Point out each Plasmodium parasite.
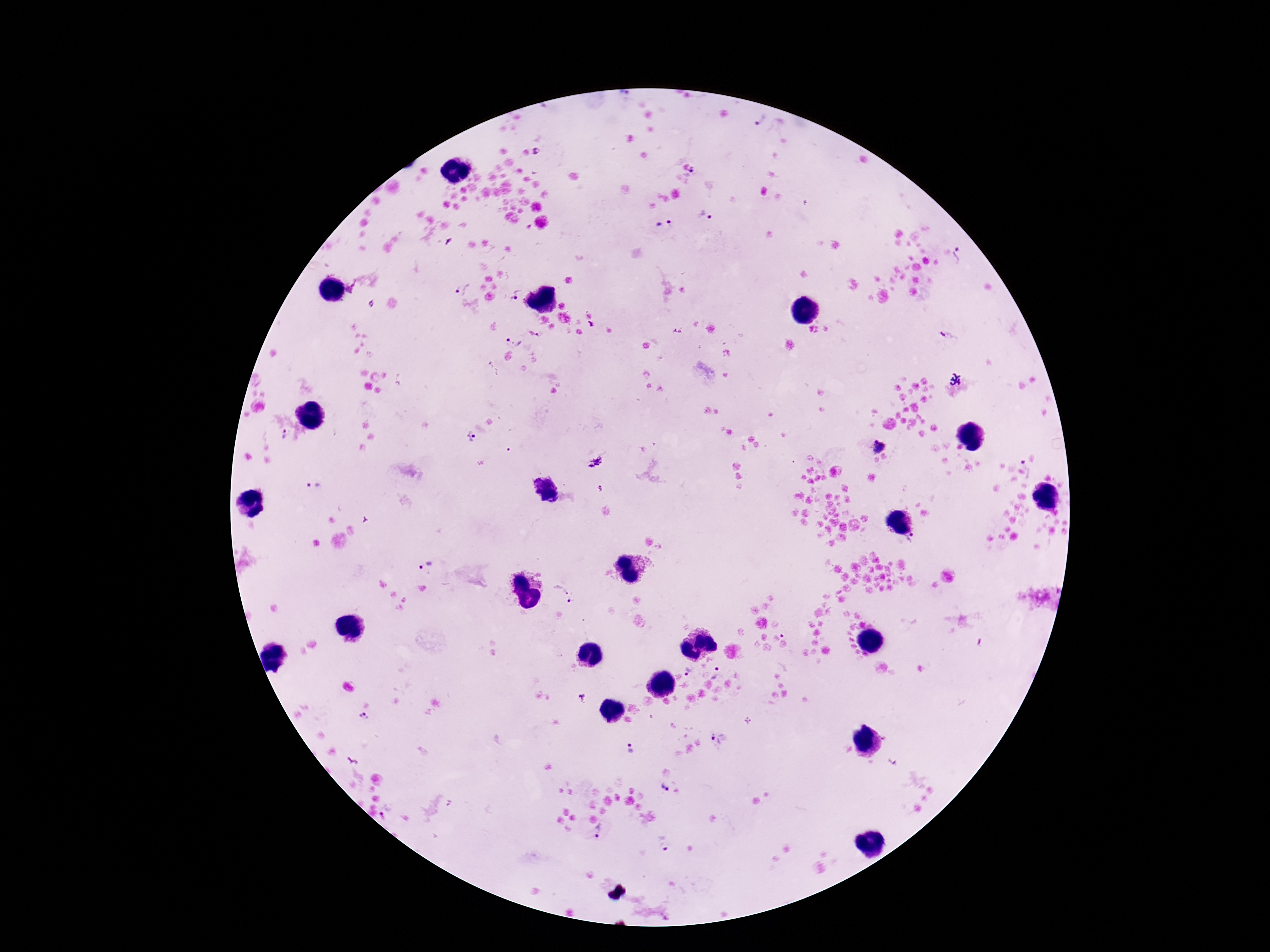
Approximate centers as {x, y} in pixels.
Plasmodium parasites: {757, 119}, {536, 151}, {692, 175}, {705, 216}, {664, 222}, {961, 256}, {352, 287}, {462, 288}, {517, 295}, {541, 333}, {948, 334}, {513, 340}, {287, 435}, {471, 438}, {879, 446}, {594, 462}, {1024, 469}, {313, 484}, {599, 489}, {912, 538}, {427, 566}, {562, 591}, {570, 602}, {783, 636}, {689, 672}, {718, 675}, {363, 717}, {719, 740}, {625, 749}, {663, 787}, {386, 807}, {600, 832}, {664, 843}.

Smartphone photograph taken through the microscope eyepiece. 100x magnification. Giemsa stain. Thick blood smear. Patient malaria status: positive. One field from this slide. Image is 1270×952 pixels.